Report the malaria status of this cell.
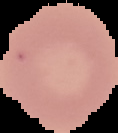

Uninfected.

Image is 118×133 pixels. Segmented cell region on a black background. From a thin blood film.